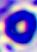
identification = white blood cell
magnification = 400x
modality = photomicrograph